Give the position of every leukocyte visible.
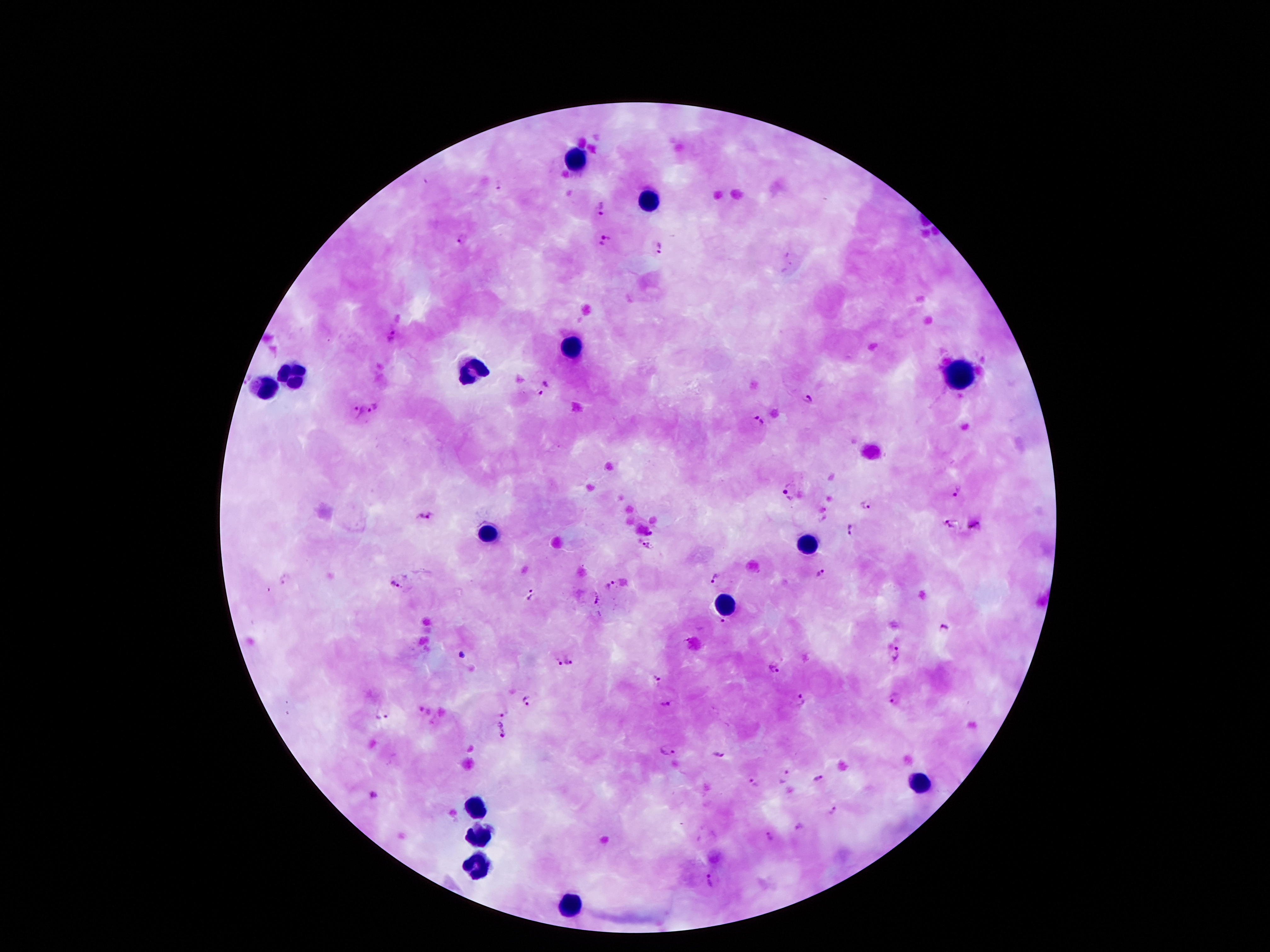

Approximate centers as [x, y] in pixels.
Leukocytes: [571, 158], [648, 200], [573, 346], [471, 370], [960, 374], [290, 377], [263, 388], [487, 536], [807, 545], [728, 602], [913, 781], [476, 810], [476, 836], [476, 865], [568, 905].

malaria parasite locations = [500, 184], [602, 209], [460, 240], [604, 240], [662, 247], [545, 388], [808, 399], [374, 410], [357, 413], [756, 422], [957, 490], [788, 491], [866, 504], [426, 515], [951, 524], [975, 526], [850, 530], [650, 532], [645, 548], [820, 574], [715, 576], [285, 579], [395, 584], [611, 586], [531, 595], [596, 599], [722, 622], [945, 629], [896, 655], [570, 661], [557, 662], [775, 669], [657, 678], [894, 699], [527, 700], [801, 701], [668, 703], [425, 710], [503, 712], [383, 715], [503, 728], [668, 751], [718, 754], [784, 777], [817, 779], [755, 784], [374, 794], [833, 811], [769, 838], [712, 878]
patient malaria status = infected with Plasmodium falciparum
image size = 1270×952 pixels
field of view = single
capture = smartphone through the microscope eyepiece
stain = Giemsa
magnification = 100x
preparation = thick peripheral-blood smear